Assess for malaria.
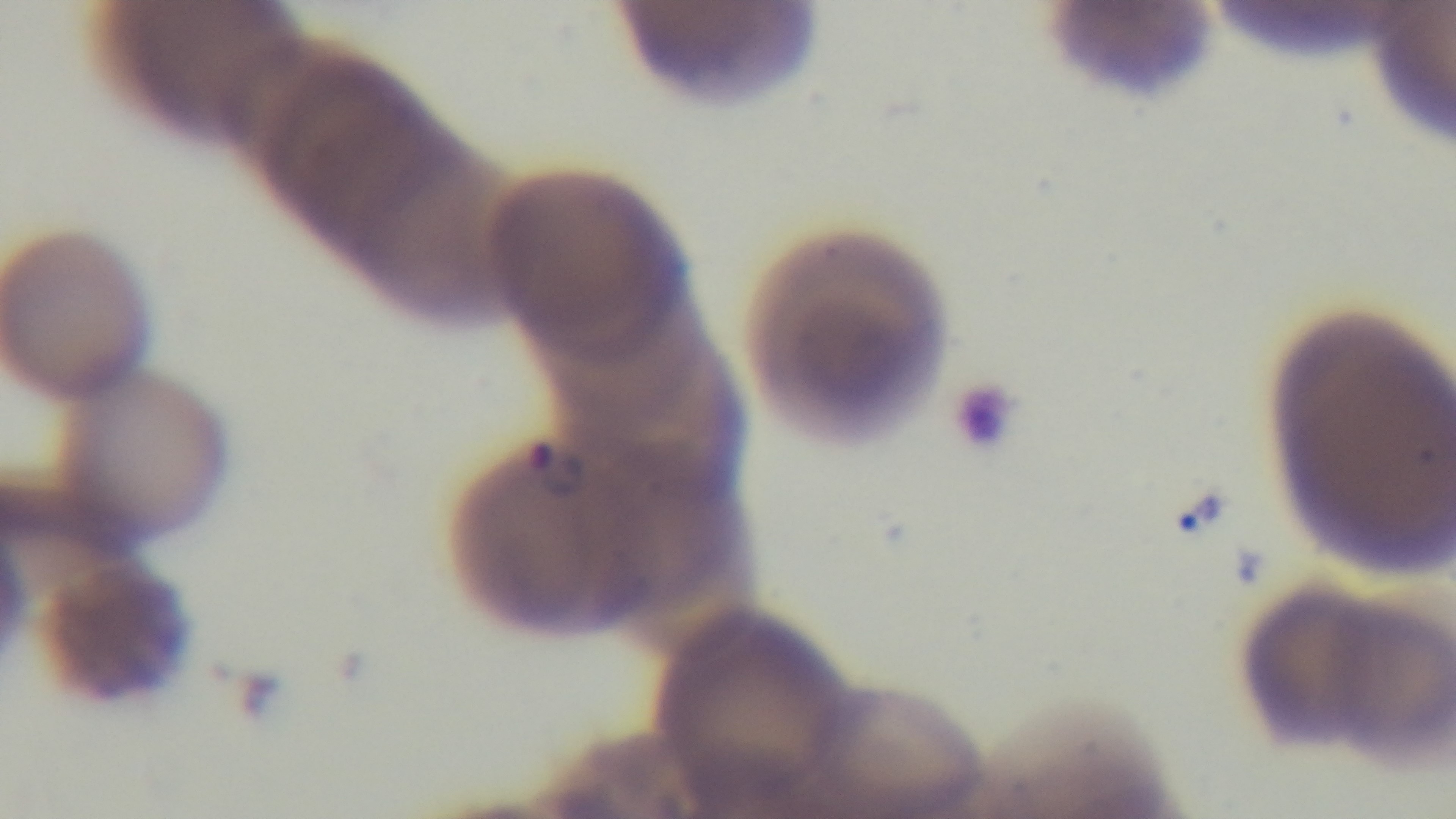
It is infected.

field of view = single
objective = 100x oil immersion
modality = light microscopy
stain = Giemsa
preparation = thin blood film
capture = mounted 4K digital camera